Report the malaria status of this cell.
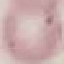

Uninfected.

Summary:
  - Image type: cell patch, automatically extracted from a larger field of view and resized to 64 × 64 pixels
  - Preparation: thin blood smear
  - Capture: smartphone through the microscope eyepiece
  - Stain: Giemsa